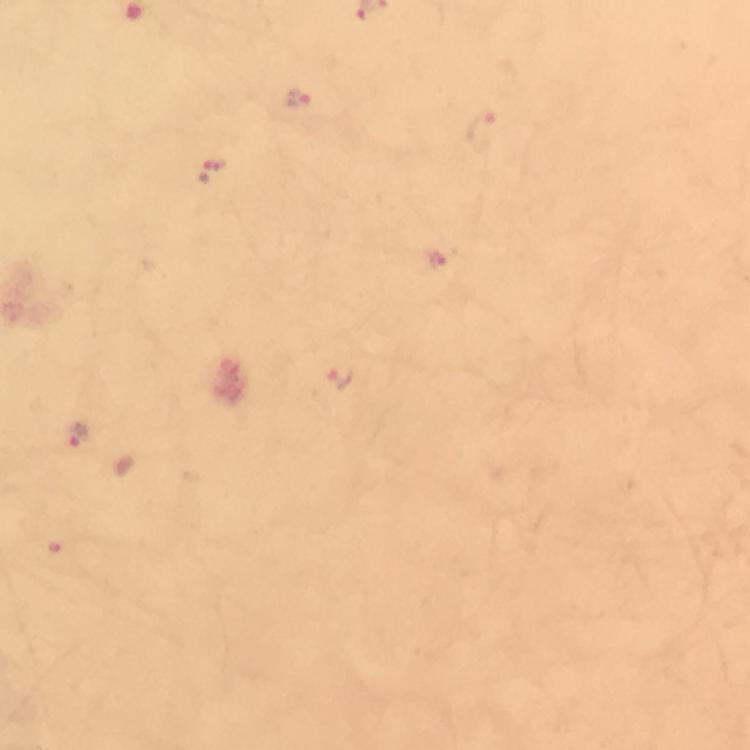
Approximate object centers, in pixels from the top-left corner.
Summary:
  - Plasmodium parasite locations: (x=298, y=98), (x=482, y=130), (x=211, y=170), (x=435, y=256), (x=340, y=379), (x=78, y=435)
  - Image size: 750×750 pixels
  - Cropped from: one field of view
  - Magnification: 100x
  - Stain: Giemsa
  - Capture: smartphone camera through the microscope
  - Context: from a malaria diagnostic workup
  - Preparation: thick smear
  - Immersion oil: used